State which parasite is depicted.
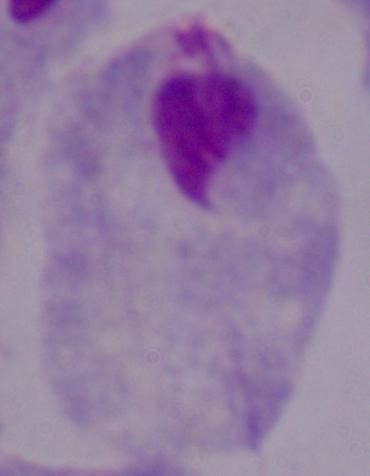

A trichomonad.

modality = photomicrograph
magnification = 1000x